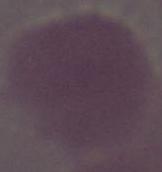
modality = micrograph
magnification = 1000x
identification = red blood cell